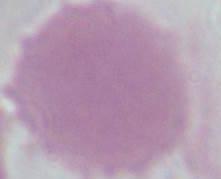
Summary:
  - Magnification: 1000x
  - Identification: erythrocyte
  - Modality: micrograph